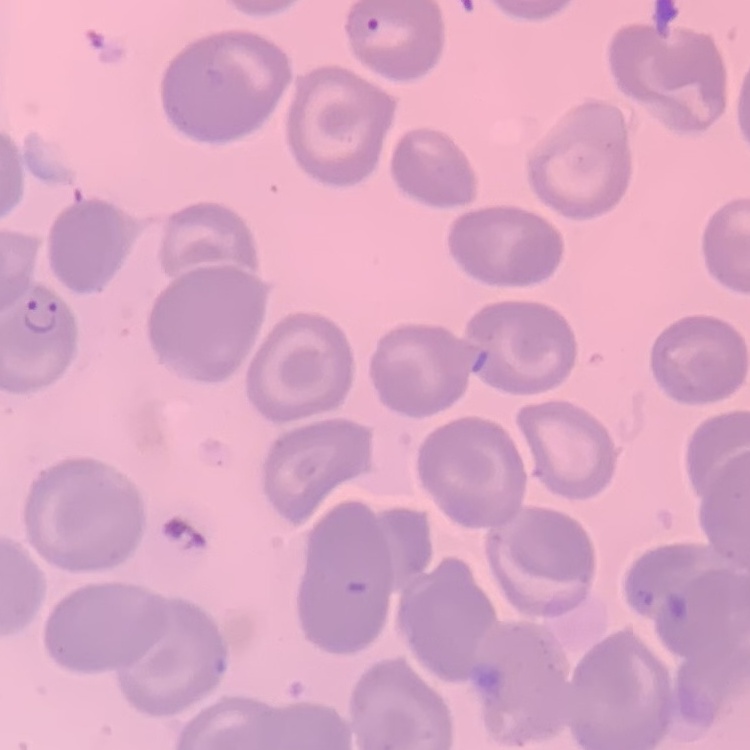 The red blood cells exhibit no rouleaux formation. Field's or Giemsa stain. Thin blood film. One tile cut from a larger photomicrograph.